Point out each leukocyte.
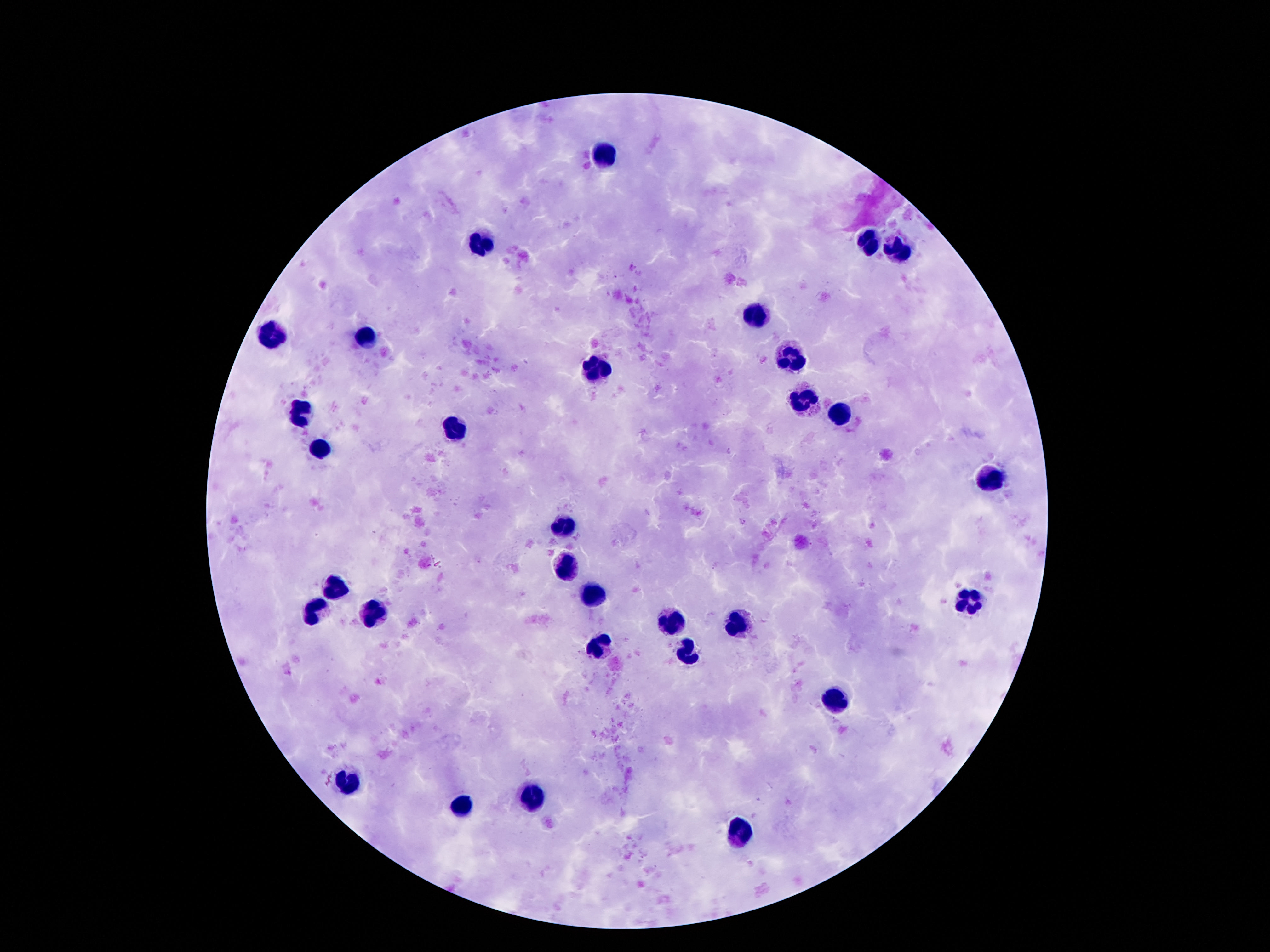
Approximate centers as [x, y] in pixels.
Leukocytes: [603, 154], [867, 242], [475, 244], [897, 248], [756, 316], [273, 334], [365, 339], [791, 358], [596, 370], [800, 399], [306, 414], [838, 416], [454, 429], [321, 450], [989, 477], [561, 526], [565, 570], [334, 587], [590, 595], [968, 600], [311, 614], [374, 615], [672, 622], [731, 623], [600, 646], [686, 656], [838, 698], [346, 781], [533, 789], [462, 803], [743, 835].

field of view = one from this slide
patient malaria status = not infected
capture = smartphone camera through the microscope eyepiece
preparation = thick blood smear
stain = Giemsa
image size = 1270×952 pixels
magnification = 100x